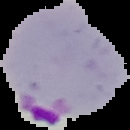

Summary:
  - Image type: segmented cell region with the area outside set to black
  - Preparation: thin blood smear
  - Image size: 130×130 pixels
  - Result: malaria parasites detected